Outline each blood parasite and name the species.
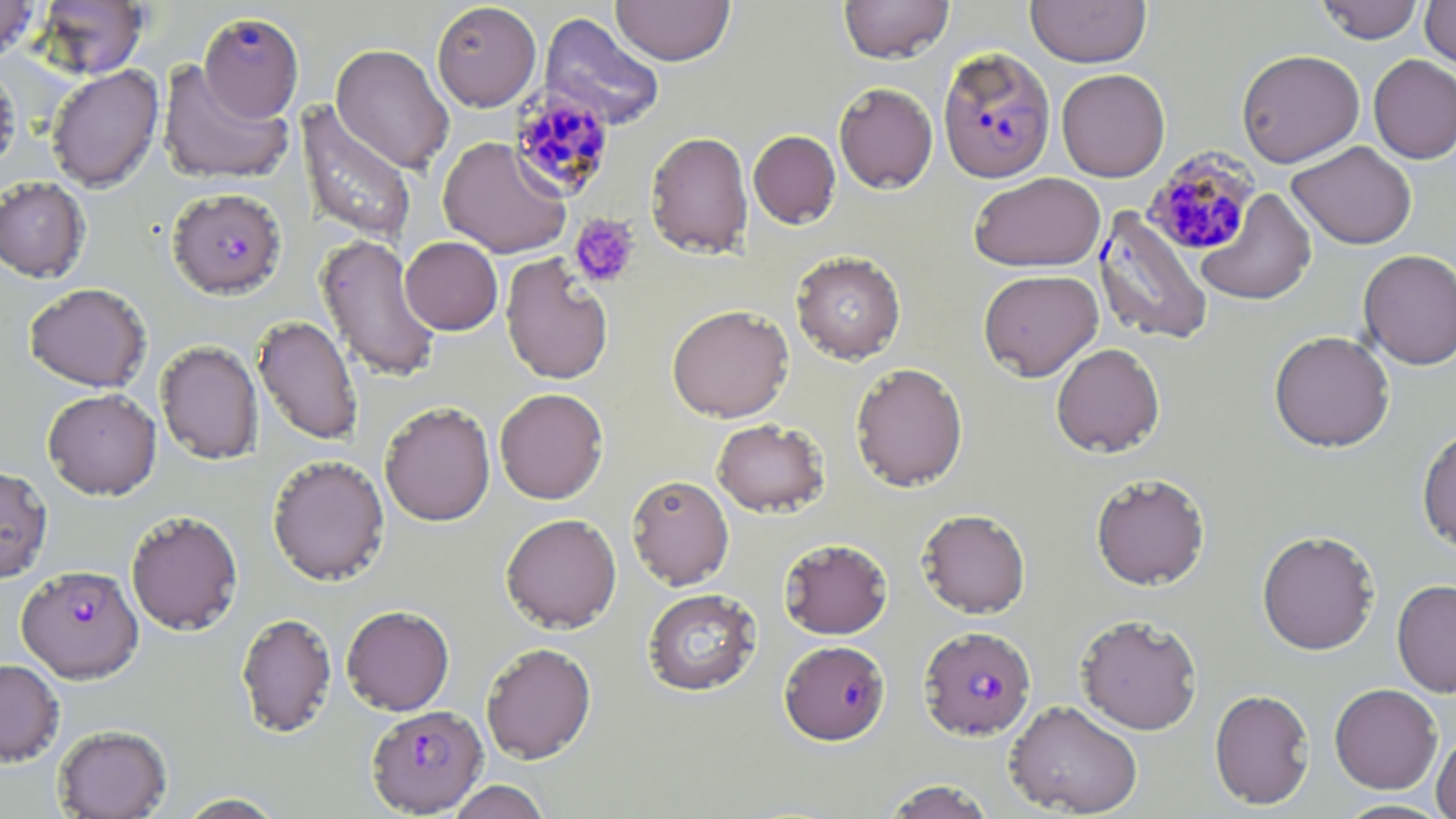

Approximate bounding boxes as (x1,y1)-(x2,y2) corner pairs in pixels.
Plasmodium falciparum-infected red blood cells: (199,12)-(304,123), (938,46)-(1056,184), (507,84)-(615,200), (1142,147)-(1261,258), (167,187)-(287,299), (1093,206)-(1213,346), (17,565)-(143,683), (919,625)-(1036,740), (779,640)-(890,745), (367,704)-(487,816).
No Plasmodium ovale, Plasmodium malariae, Plasmodium vivax, Babesia divergens, or Trypanosoma brucei observed.

Summary:
  - Uninfected red blood cell locations: (0,0)-(40,62), (610,0)-(735,66), (839,0)-(953,64), (1026,0)-(1151,67), (1316,0)-(1424,43), (1420,0)-(1456,70), (33,1)-(150,78), (431,2)-(541,111), (540,12)-(665,130), (331,44)-(454,174), (1236,49)-(1365,167), (1368,55)-(1456,164), (157,59)-(294,186), (0,62)-(22,176), (46,65)-(164,192), (1056,68)-(1170,181), (833,82)-(938,194), (295,101)-(418,247), (748,130)-(841,229), (645,131)-(753,259), (437,136)-(572,259), (1287,141)-(1417,249), (968,171)-(1105,272), (0,177)-(91,283), (1196,189)-(1317,306), (315,233)-(442,383), (400,236)-(503,335), (1358,248)-(1456,370), (791,251)-(906,364), (500,254)-(614,385), (978,269)-(1103,380), (24,283)-(152,392), (666,304)-(794,422), (252,314)-(364,445), (1269,330)-(1395,452), (155,340)-(263,465), (1051,342)-(1165,458), (850,362)-(969,491), (43,387)-(162,500), (494,387)-(609,504), (379,400)-(495,526), (711,418)-(830,517), (1417,424)-(1456,553), (267,454)-(390,586), (0,465)-(52,583), (1090,472)-(1210,591), (626,474)-(734,590), (917,508)-(1031,618), (126,510)-(243,635), (500,513)-(622,633), (1256,529)-(1380,655), (778,538)-(893,639), (1392,578)-(1456,697), (642,588)-(761,696), (341,605)-(454,715), (236,612)-(337,738), (1076,613)-(1203,734), (481,641)-(597,764), (0,658)-(65,766), (1329,683)-(1442,794), (1209,688)-(1315,809), (1004,699)-(1143,817), (53,724)-(172,819), (1432,729)-(1456,819), (446,780)-(552,819), (880,780)-(998,819), (173,793)-(288,818), (1334,799)-(1451,818)
  - Platelet locations: (568,214)-(641,289)
  - Slide-level diagnosis: Plasmodium falciparum
  - Field of view: one of a larger specimen
  - Magnification: 1000x
  - Modality: optical microscopy
  - Stain: May-Grünwald-Giemsa
  - Image size: 1456×819 pixels
  - Preparation: thin blood smear